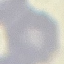
Result: no malaria parasites detected. Automatically extracted cell patch, resized to 64 × 64 pixels. Thin blood smear. Acquired by smartphone through the microscope eyepiece. Giemsa-stained preparation.